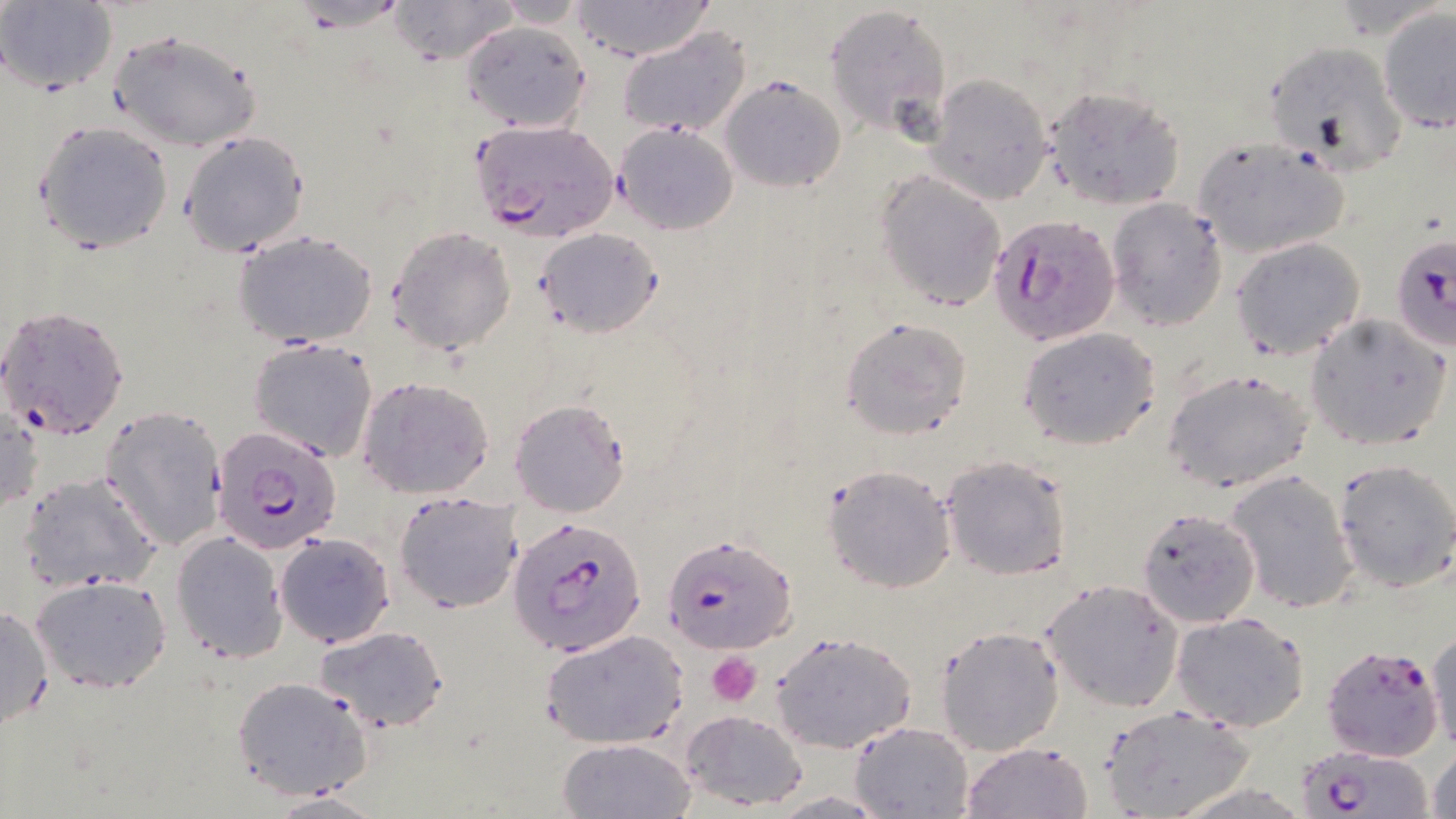
Summary:
  - Coordinate format: approximate bounding boxes as [x1, y1, x2, y2] in pixels
  - Platelet locations: [707, 652, 761, 707]
  - Uninfected red blood cell locations: [389, 0, 518, 66], [489, 0, 593, 27], [567, 0, 719, 61], [0, 1, 117, 93], [825, 4, 951, 139], [1378, 8, 1456, 134], [463, 18, 591, 133], [617, 27, 752, 139], [108, 29, 261, 152], [1264, 39, 1407, 173], [927, 73, 1054, 203], [721, 77, 844, 194], [1042, 85, 1185, 209], [32, 118, 175, 254], [614, 122, 740, 234], [179, 129, 310, 258], [1190, 135, 1351, 259], [874, 170, 1007, 312], [1106, 197, 1230, 332], [387, 226, 516, 357], [536, 226, 663, 337], [235, 232, 378, 349], [1230, 236, 1365, 359], [0, 304, 130, 441], [1304, 313, 1451, 452], [839, 317, 971, 440], [1018, 327, 1161, 450], [249, 337, 379, 463], [1163, 367, 1314, 493], [356, 376, 495, 499], [508, 400, 629, 519], [1, 404, 42, 522], [100, 405, 230, 552], [941, 453, 1073, 579], [1333, 458, 1456, 591], [822, 463, 957, 594], [19, 470, 162, 593], [1226, 470, 1359, 615], [393, 490, 524, 614], [1135, 506, 1261, 627], [171, 531, 288, 663], [274, 533, 395, 647], [30, 574, 172, 694], [1041, 579, 1183, 713], [0, 605, 54, 734], [1171, 612, 1311, 732], [937, 625, 1065, 756], [315, 626, 449, 731], [540, 629, 689, 749], [1428, 629, 1456, 755], [771, 631, 917, 753], [231, 675, 373, 799], [1099, 706, 1253, 819], [680, 709, 808, 811], [850, 720, 975, 819], [557, 738, 696, 819], [959, 740, 1094, 819], [1427, 744, 1456, 819], [767, 790, 893, 817], [268, 792, 387, 819]
  - Plasmodium falciparum-infected red blood cell locations: [469, 120, 620, 243], [988, 213, 1119, 346], [1391, 231, 1454, 350], [213, 428, 344, 555], [507, 515, 648, 658], [662, 534, 795, 653], [1320, 643, 1446, 762], [1297, 745, 1430, 818]
  - Slide-level diagnosis: Plasmodium falciparum
  - Modality: light microscopy
  - Magnification: 1000x
  - Field of view: one of a larger specimen
  - Stain: May-Grünwald-Giemsa
  - Image size: 1456×819 pixels
  - Preparation: thin blood film